Locate and identify every blood parasite.
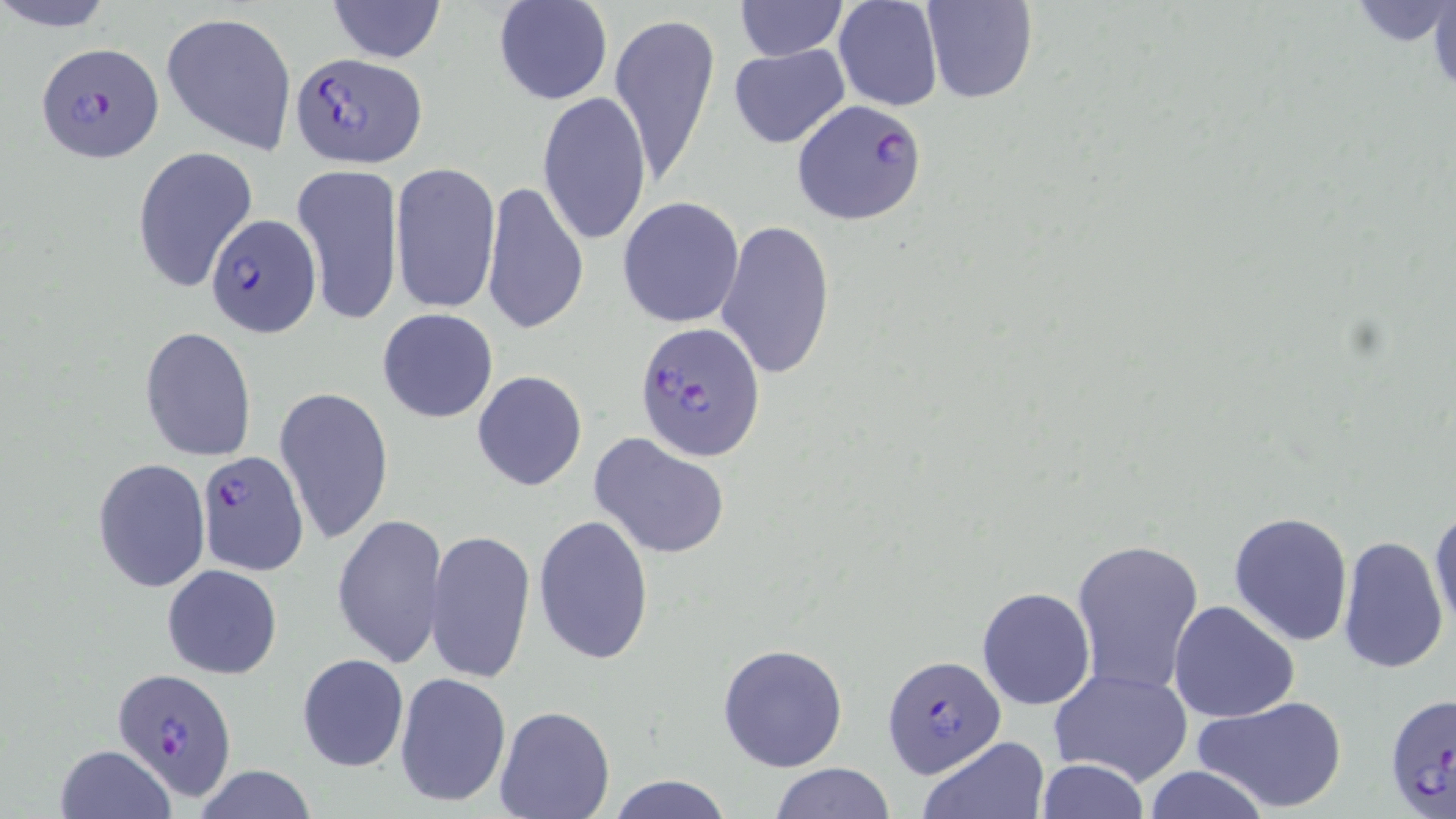
Approximate bounding boxes as (x1, y1, x2, y2) in pixels.
Plasmodium falciparum-infected red blood cells: (35, 41, 163, 162), (290, 51, 424, 166), (792, 98, 929, 226), (205, 213, 319, 337), (634, 321, 767, 461), (195, 449, 307, 576), (882, 653, 1006, 776), (112, 668, 239, 799), (1384, 689, 1454, 819).
No Plasmodium ovale, Plasmodium malariae, Plasmodium vivax, Babesia divergens, or Trypanosoma brucei observed.

Summary:
  - Uninfected red blood cell locations: (0, 0, 118, 32), (493, 0, 613, 105), (922, 0, 1037, 104), (1426, 0, 1456, 98), (327, 1, 445, 64), (734, 1, 847, 62), (832, 1, 944, 111), (1351, 3, 1454, 45), (160, 10, 297, 155), (610, 11, 721, 191), (728, 44, 850, 147), (537, 91, 652, 247), (131, 145, 256, 295), (390, 160, 501, 316), (292, 163, 403, 325), (482, 179, 589, 338), (617, 196, 745, 328), (715, 219, 835, 381), (376, 308, 499, 424), (140, 326, 257, 460), (471, 370, 587, 492), (274, 386, 394, 546), (589, 432, 731, 562), (92, 457, 211, 594), (1429, 507, 1455, 634), (1228, 511, 1355, 648), (334, 513, 448, 670), (532, 514, 654, 666), (426, 526, 536, 686), (1336, 535, 1450, 674), (1069, 537, 1205, 695), (161, 564, 283, 680), (977, 586, 1096, 711), (1168, 600, 1299, 724), (718, 642, 849, 773), (296, 653, 409, 773), (1047, 667, 1193, 787), (395, 672, 511, 806), (1193, 694, 1349, 816), (493, 704, 615, 818), (918, 735, 1051, 819), (53, 744, 177, 819), (1036, 758, 1149, 818), (768, 762, 895, 818), (1141, 765, 1272, 819), (193, 766, 319, 819), (607, 774, 733, 818)
  - Slide-level diagnosis: Plasmodium falciparum
  - Preparation: thin blood film
  - Field of view: single
  - Modality: light microscopy
  - Magnification: 1000x
  - Stain: May-Grünwald-Giemsa
  - Image size: 1456×819 pixels